Point out each leukocyte.
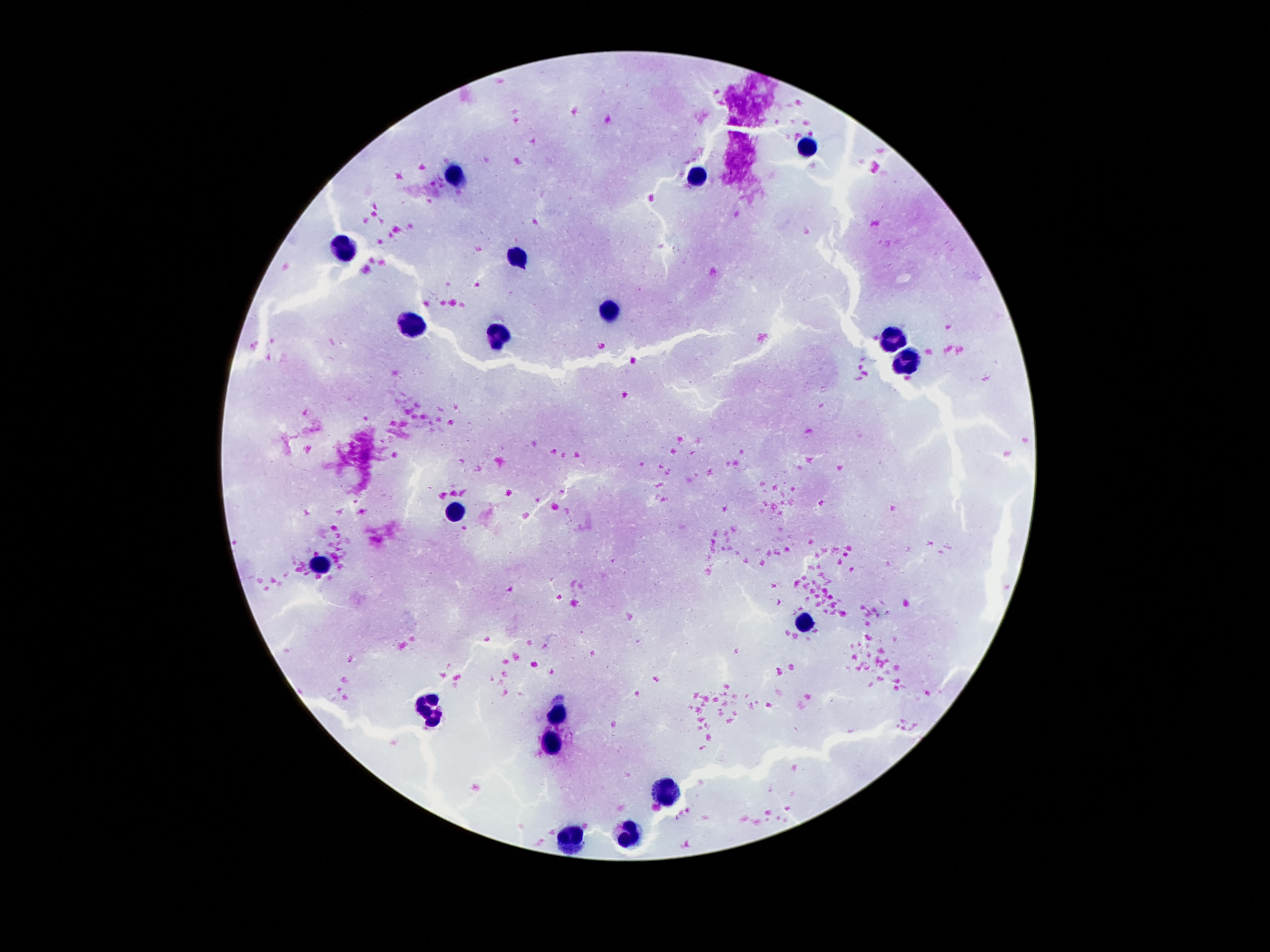

Approximate centers as (x, y) in pixels.
Leukocytes: (808, 149), (697, 175), (455, 176), (345, 249), (520, 259), (610, 312), (414, 325), (502, 335), (892, 341), (908, 366), (455, 510), (320, 562), (804, 623), (431, 708), (556, 715), (550, 745), (669, 792), (630, 834), (571, 841).

Thick blood film. Patient malaria status: uninfected. Photographed through the microscope eyepiece with a smartphone camera. Single field of view. Image is 1270×952 pixels. 100x magnification. Giemsa stain.